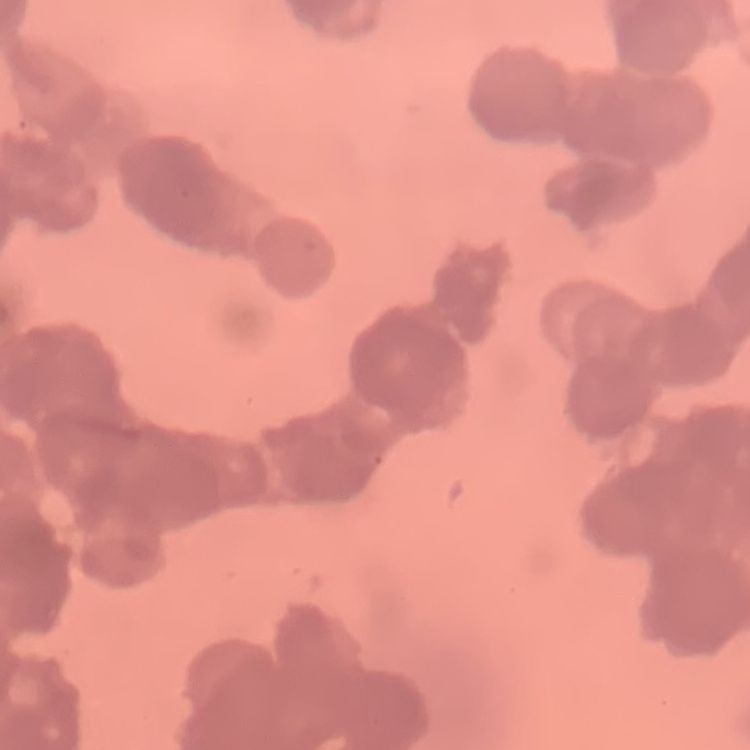
{
  "erythrocyte_morphology": "rouleaux formation",
  "image_type": "square crop of a larger photomicrograph",
  "stain": "Field's or Giemsa",
  "preparation": "thin peripheral smear"
}